Describe the morphology of the erythrocytes.
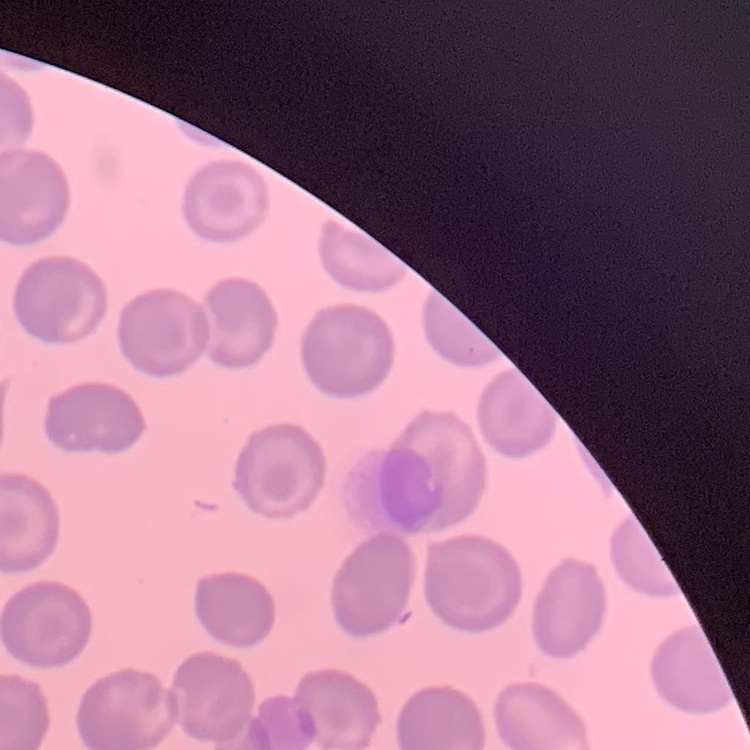

They show no rouleaux formation.

Summary:
  - Stain: Field's or Giemsa
  - Image type: one tile cut from a larger photomicrograph
  - Preparation: thin blood smear